Outline each uninfected red blood cell.
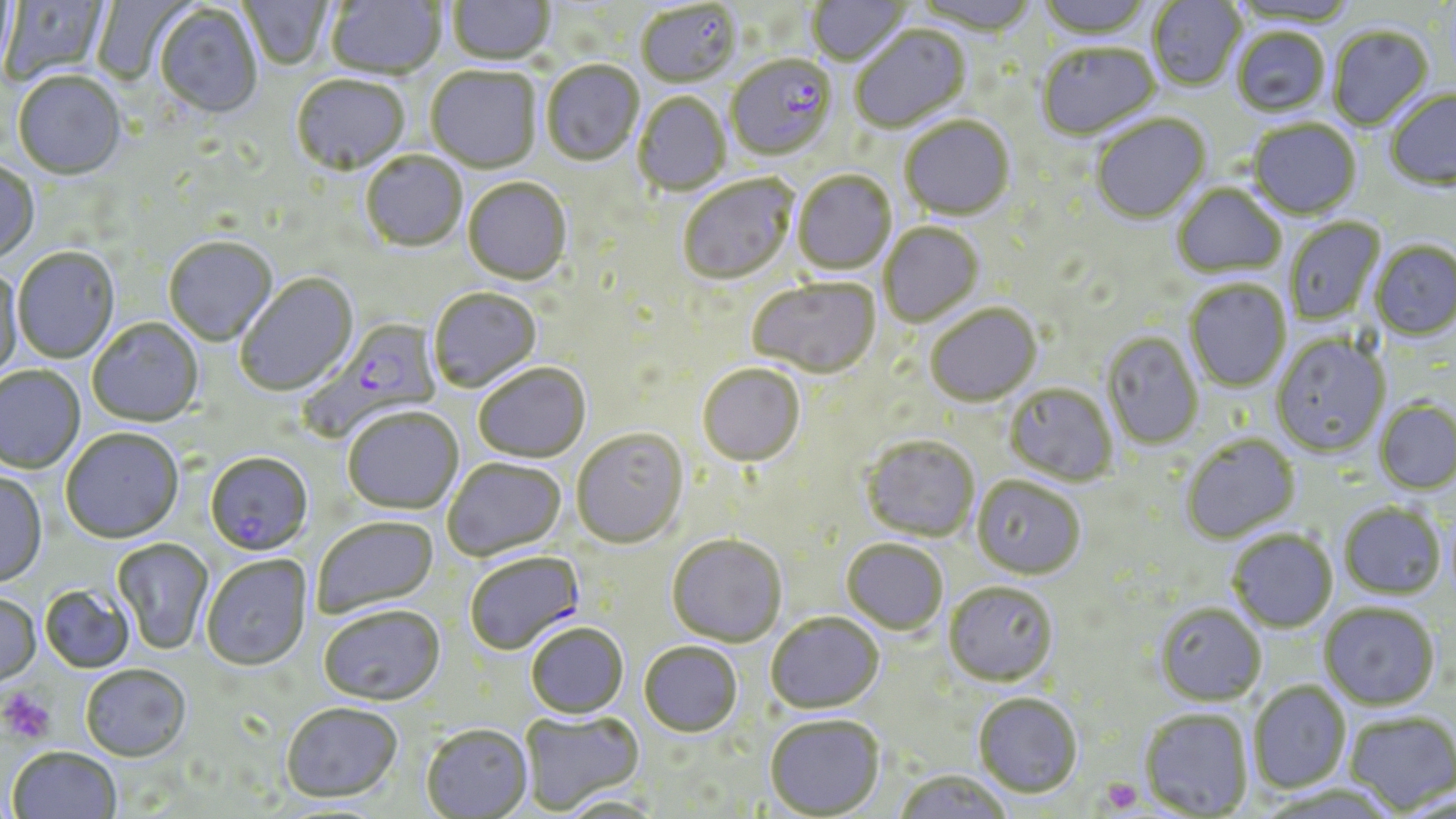
Approximate bounding boxes as named x1/y1/x2/y2 corners in pixels.
Uninfected red blood cells: (x1=0, y1=0, x2=110, y2=86), (x1=0, y1=0, x2=20, y2=85), (x1=91, y1=0, x2=193, y2=85), (x1=238, y1=0, x2=333, y2=71), (x1=326, y1=0, x2=445, y2=81), (x1=448, y1=0, x2=555, y2=67), (x1=807, y1=0, x2=910, y2=69), (x1=908, y1=0, x2=1038, y2=37), (x1=1035, y1=0, x2=1154, y2=41), (x1=1147, y1=0, x2=1245, y2=92), (x1=1228, y1=0, x2=1358, y2=28), (x1=636, y1=3, x2=742, y2=90), (x1=155, y1=6, x2=262, y2=120), (x1=851, y1=26, x2=972, y2=134), (x1=1329, y1=27, x2=1434, y2=131), (x1=1232, y1=29, x2=1331, y2=118), (x1=1038, y1=44, x2=1161, y2=142), (x1=541, y1=62, x2=644, y2=167), (x1=426, y1=68, x2=541, y2=175), (x1=13, y1=73, x2=126, y2=182), (x1=292, y1=76, x2=410, y2=178), (x1=1385, y1=90, x2=1456, y2=191), (x1=633, y1=93, x2=731, y2=197), (x1=1092, y1=115, x2=1211, y2=226), (x1=900, y1=117, x2=1015, y2=222), (x1=1249, y1=120, x2=1361, y2=221), (x1=361, y1=152, x2=467, y2=254), (x1=0, y1=161, x2=40, y2=265), (x1=792, y1=172, x2=897, y2=275), (x1=678, y1=176, x2=798, y2=285), (x1=463, y1=180, x2=572, y2=287), (x1=1172, y1=185, x2=1286, y2=279), (x1=1284, y1=216, x2=1385, y2=326), (x1=879, y1=223, x2=984, y2=327), (x1=164, y1=238, x2=278, y2=347), (x1=1370, y1=240, x2=1456, y2=341), (x1=13, y1=249, x2=120, y2=364), (x1=0, y1=266, x2=24, y2=382), (x1=235, y1=274, x2=359, y2=398), (x1=747, y1=279, x2=880, y2=379), (x1=1184, y1=279, x2=1291, y2=392), (x1=428, y1=288, x2=542, y2=393), (x1=926, y1=305, x2=1042, y2=407), (x1=87, y1=318, x2=205, y2=429), (x1=1102, y1=333, x2=1203, y2=450), (x1=1271, y1=333, x2=1390, y2=457), (x1=474, y1=364, x2=591, y2=463), (x1=698, y1=364, x2=805, y2=467), (x1=0, y1=367, x2=85, y2=474), (x1=1005, y1=384, x2=1118, y2=487), (x1=1375, y1=399, x2=1456, y2=495), (x1=342, y1=408, x2=464, y2=515), (x1=60, y1=429, x2=183, y2=545), (x1=571, y1=429, x2=689, y2=549), (x1=1181, y1=433, x2=1301, y2=544), (x1=860, y1=435, x2=980, y2=542), (x1=443, y1=457, x2=566, y2=561), (x1=0, y1=472, x2=48, y2=590), (x1=972, y1=476, x2=1085, y2=580), (x1=1339, y1=502, x2=1446, y2=599), (x1=312, y1=516, x2=440, y2=619), (x1=1228, y1=530, x2=1338, y2=632), (x1=666, y1=534, x2=786, y2=646), (x1=112, y1=538, x2=214, y2=655), (x1=842, y1=539, x2=948, y2=634), (x1=201, y1=556, x2=313, y2=672), (x1=944, y1=580, x2=1059, y2=686), (x1=40, y1=585, x2=134, y2=674), (x1=0, y1=594, x2=42, y2=687), (x1=1320, y1=602, x2=1440, y2=709), (x1=1155, y1=603, x2=1266, y2=705), (x1=318, y1=607, x2=445, y2=708), (x1=766, y1=613, x2=884, y2=714), (x1=526, y1=623, x2=629, y2=718), (x1=639, y1=641, x2=742, y2=736), (x1=81, y1=666, x2=191, y2=763), (x1=1249, y1=680, x2=1351, y2=792), (x1=973, y1=693, x2=1082, y2=798), (x1=281, y1=703, x2=403, y2=804), (x1=1140, y1=708, x2=1254, y2=818), (x1=520, y1=709, x2=645, y2=815), (x1=1345, y1=710, x2=1455, y2=814), (x1=765, y1=714, x2=885, y2=818), (x1=421, y1=725, x2=533, y2=818), (x1=7, y1=748, x2=122, y2=819), (x1=893, y1=770, x2=1012, y2=819), (x1=556, y1=795, x2=664, y2=818).

slide-level diagnosis = Plasmodium falciparum
field of view = single
magnification = 1000x
modality = optical microscopy
preparation = thin blood smear
image size = 1456×819 pixels
stain = May-Grünwald-Giemsa
platelet locations = approximate bounding boxes as named x1/y1/x2/y2 corners in pixels: (x1=0, y1=688, x2=56, y2=745), (x1=1098, y1=776, x2=1143, y2=815)
Plasmodium falciparum-infected red blood cell locations = approximate bounding boxes as named x1/y1/x2/y2 corners in pixels: (x1=726, y1=57, x2=838, y2=162), (x1=298, y1=317, x2=442, y2=442), (x1=205, y1=453, x2=314, y2=558), (x1=464, y1=552, x2=585, y2=655)